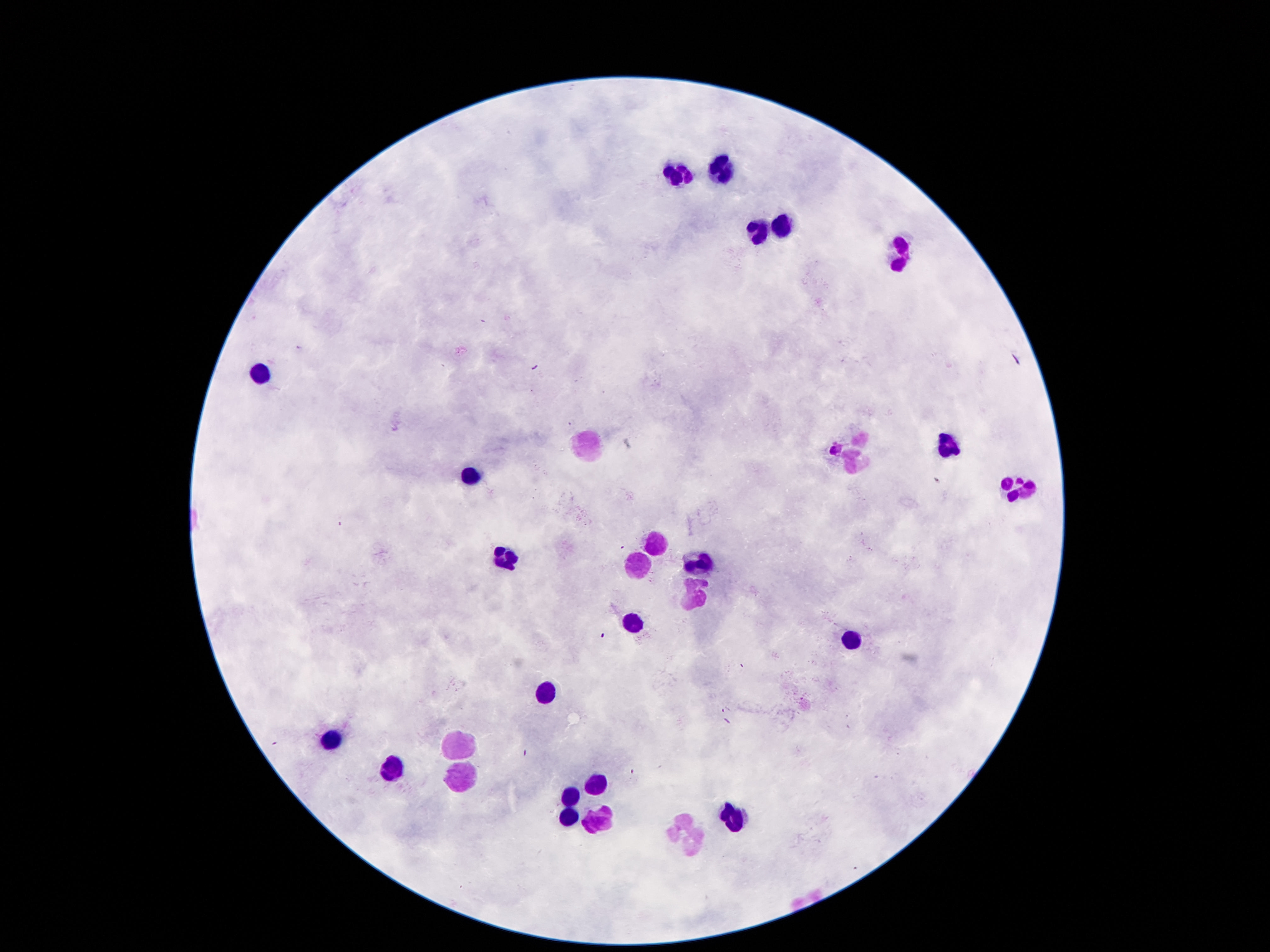

Approximate centers as (x, y) in pixels. Leukocyte locations: (720, 171), (679, 177), (784, 223), (756, 232), (903, 258), (262, 377), (587, 442), (852, 447), (948, 447), (468, 475), (1019, 486), (657, 543), (507, 557), (636, 562), (701, 566), (690, 597), (633, 621), (848, 638), (549, 689), (331, 739), (457, 743), (390, 766), (461, 775), (591, 786), (570, 794), (568, 812), (728, 815), (598, 821), (688, 838). Patient malaria status: not infected. Image is 1270×952 pixels. Thick peripheral-blood smear. Smartphone photograph taken through the microscope eyepiece. Giemsa stain. 100x magnification. One field from this slide.